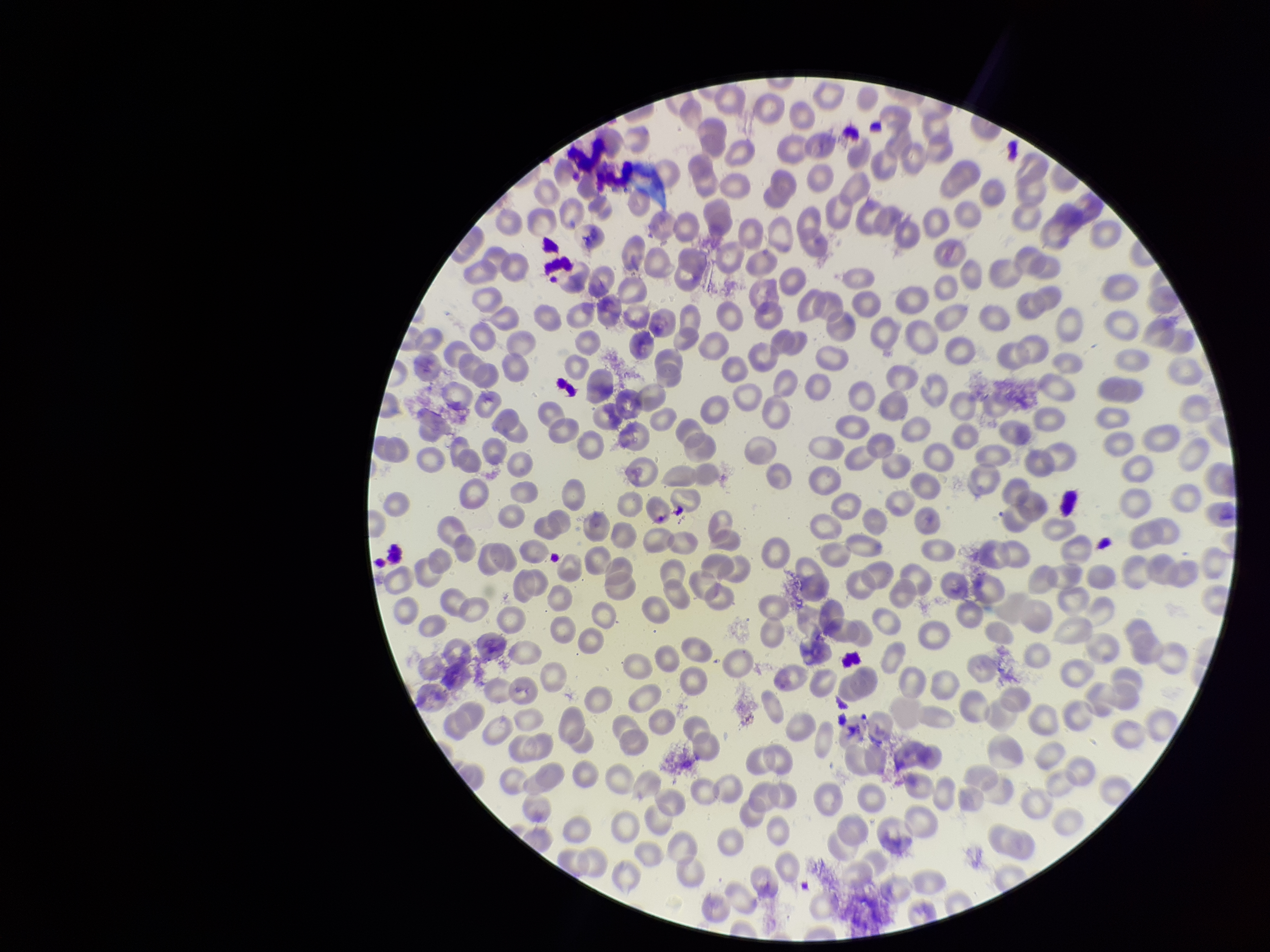

Summary:
  - Field of view: single
  - Preparation: thin smear
  - Patient malaria status: negative
  - Parasitized red blood cells: none identified
  - Capture: smartphone photograph through the microscope eyepiece
  - Stain: Giemsa
  - Image size: 1270×952 pixels
  - Parasitized red blood cell count: 0
  - Red blood cell count: 276